Give the extent of all Trypanosoma brucei.
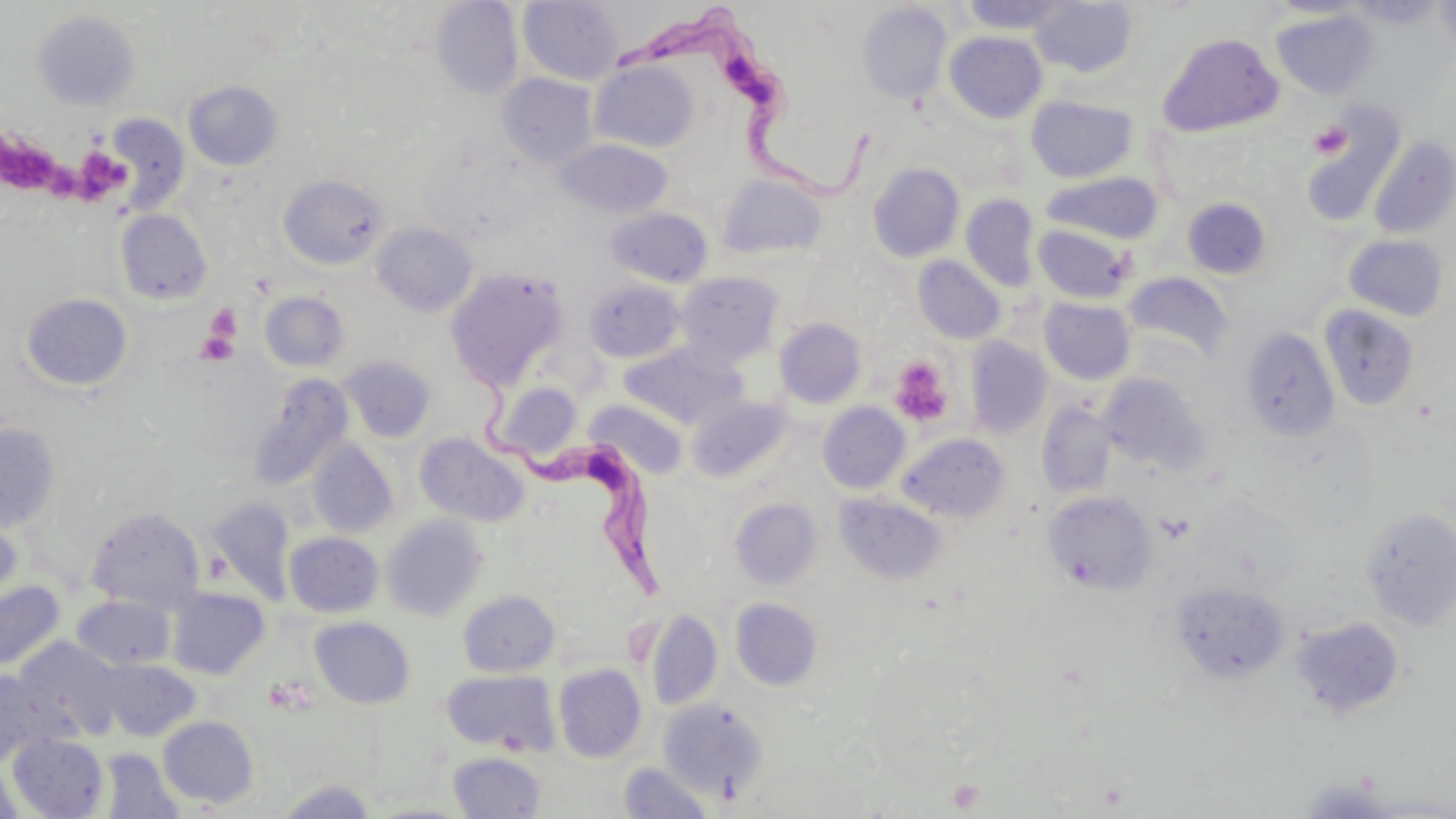

Approximate bounding boxes as (x1, y1, x2, y2) in pixels.
Trypanosoma brucei: (613, 6, 875, 198), (465, 380, 669, 600).

Summary:
  - Platelet locations: (1308, 120, 1351, 160), (2, 127, 67, 196), (76, 140, 138, 202), (204, 306, 240, 345), (195, 331, 239, 365), (889, 356, 953, 426), (264, 677, 313, 715), (947, 779, 985, 813)
  - Uninfected red blood cell locations: (518, 0, 623, 85), (960, 0, 1072, 34), (1267, 0, 1370, 18), (1349, 0, 1446, 27), (1436, 0, 1456, 57), (431, 1, 524, 99), (1030, 1, 1137, 77), (857, 3, 952, 103), (1272, 9, 1378, 99), (31, 10, 141, 111), (944, 31, 1047, 123), (1158, 31, 1284, 136), (591, 60, 700, 152), (497, 73, 598, 167), (183, 81, 283, 170), (1026, 95, 1138, 183), (1301, 104, 1406, 225), (107, 115, 190, 211), (1369, 136, 1456, 240), (554, 140, 673, 219), (868, 162, 965, 263), (1043, 172, 1163, 244), (279, 174, 389, 269), (718, 174, 828, 261), (961, 194, 1040, 291), (1182, 197, 1272, 279), (606, 207, 713, 287), (115, 209, 212, 305), (372, 222, 478, 316), (1035, 225, 1133, 304), (1343, 234, 1450, 322), (913, 256, 1006, 344), (446, 268, 568, 389), (676, 272, 783, 367), (1123, 272, 1234, 362), (584, 278, 685, 363), (260, 291, 349, 372), (21, 293, 133, 391), (1039, 297, 1135, 384), (1320, 304, 1420, 410), (775, 318, 866, 408), (1241, 327, 1340, 442), (965, 337, 1053, 438), (620, 342, 746, 429), (339, 355, 437, 443), (1098, 373, 1210, 476), (248, 374, 354, 489), (491, 381, 582, 463), (688, 396, 792, 483), (585, 399, 688, 479), (1035, 400, 1119, 499), (818, 402, 910, 494), (0, 422, 62, 532), (415, 432, 529, 527), (898, 432, 1010, 522), (305, 438, 399, 539), (1043, 489, 1158, 595), (836, 493, 948, 585), (204, 496, 297, 605), (730, 499, 822, 590), (0, 505, 23, 606), (86, 506, 206, 612), (1360, 507, 1456, 630), (381, 514, 487, 621), (284, 531, 384, 617), (0, 580, 65, 671), (1172, 581, 1289, 683), (166, 588, 270, 680), (458, 589, 561, 676), (72, 595, 176, 670), (730, 597, 823, 691), (646, 610, 724, 710), (1291, 616, 1406, 718), (310, 617, 415, 708), (14, 637, 125, 741), (98, 658, 199, 740), (553, 663, 647, 763), (0, 668, 63, 766), (441, 669, 560, 755), (658, 698, 769, 799), (157, 715, 259, 808), (8, 733, 109, 818), (98, 748, 184, 818), (448, 751, 547, 818), (0, 762, 22, 819), (618, 762, 714, 818), (1295, 777, 1399, 818), (275, 779, 377, 818), (367, 801, 478, 818)
  - Slide-level diagnosis: Trypanosoma brucei
  - Modality: light microscopy
  - Magnification: 1000x
  - Image size: 1456×819 pixels
  - Field of view: single
  - Stain: May-Grünwald-Giemsa
  - Preparation: thin blood film